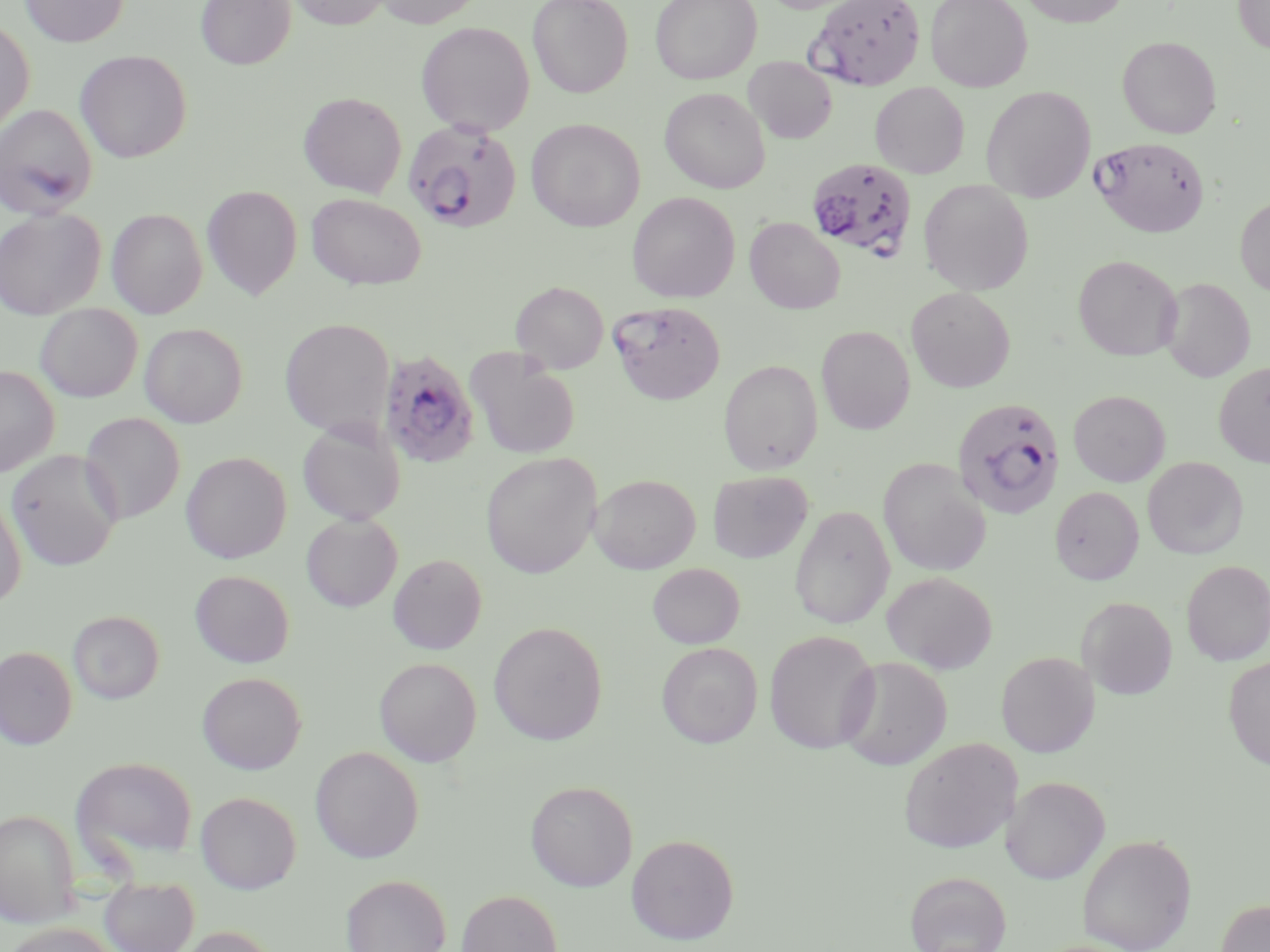

Summary:
  - Coordinate format: approximate bounding boxes as [x1, y1, x2, y2] in pixels
  - Plasmodium falciparum-infected red blood cell locations: [806, 0, 926, 90], [402, 119, 523, 233], [1091, 136, 1210, 238], [806, 158, 918, 261], [609, 300, 726, 404], [377, 350, 481, 469], [951, 396, 1065, 520]
  - Uninfected red blood cell locations: [21, 0, 128, 47], [196, 0, 296, 69], [286, 0, 391, 29], [373, 0, 483, 28], [528, 0, 633, 97], [650, 0, 762, 85], [925, 0, 1032, 92], [1019, 0, 1130, 27], [1233, 0, 1270, 54], [0, 17, 35, 137], [416, 21, 535, 136], [1118, 36, 1222, 138], [75, 50, 191, 163], [743, 57, 837, 143], [870, 82, 970, 178], [981, 86, 1096, 203], [659, 87, 770, 193], [298, 92, 407, 197], [0, 103, 98, 219], [526, 118, 645, 231], [919, 179, 1034, 294], [202, 185, 302, 299], [627, 191, 740, 303], [306, 193, 426, 289], [1235, 197, 1270, 297], [0, 208, 105, 319], [106, 208, 207, 318], [744, 217, 845, 314], [1073, 254, 1182, 361], [1160, 277, 1254, 382], [511, 280, 609, 374], [906, 287, 1015, 392], [35, 303, 143, 402], [279, 318, 395, 437], [139, 323, 247, 427], [816, 325, 915, 434], [466, 349, 581, 460], [718, 358, 823, 474], [1214, 362, 1270, 468], [0, 365, 59, 477], [1068, 389, 1170, 486], [80, 412, 185, 524], [297, 419, 406, 526], [6, 450, 122, 571], [181, 452, 291, 563], [480, 452, 601, 579], [1143, 456, 1248, 559], [877, 458, 991, 577], [707, 470, 813, 563], [590, 474, 700, 573], [1050, 486, 1144, 585], [0, 492, 26, 608], [790, 505, 895, 629], [301, 514, 402, 612], [388, 553, 487, 655], [1181, 560, 1270, 666], [647, 563, 744, 649], [190, 569, 294, 668], [881, 571, 997, 674], [1078, 597, 1178, 700], [68, 610, 163, 704], [489, 621, 608, 745], [764, 630, 881, 754], [656, 642, 762, 748], [0, 646, 77, 750], [996, 651, 1099, 757], [837, 657, 952, 770], [1223, 657, 1270, 770], [375, 658, 481, 766], [197, 672, 306, 774], [899, 737, 1021, 853], [310, 746, 424, 863], [71, 756, 199, 866], [1002, 776, 1110, 884], [525, 780, 638, 891], [195, 791, 301, 893], [0, 809, 80, 926], [626, 834, 739, 945], [1078, 834, 1196, 951], [904, 871, 1012, 952], [341, 874, 451, 952], [99, 877, 199, 952], [457, 889, 562, 952], [1215, 898, 1270, 952], [4, 923, 118, 952], [172, 925, 279, 952]
  - Slide-level diagnosis: Plasmodium falciparum
  - Field of view: one of a larger specimen
  - Modality: light microscopy
  - Magnification: 1000x
  - Stain: May-Grünwald-Giemsa
  - Image size: 1270×952 pixels
  - Preparation: thin blood smear